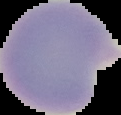 From a thin blood film. Segmented cell region on a black background. Malaria status: parasitized. Image is 121×115 pixels.